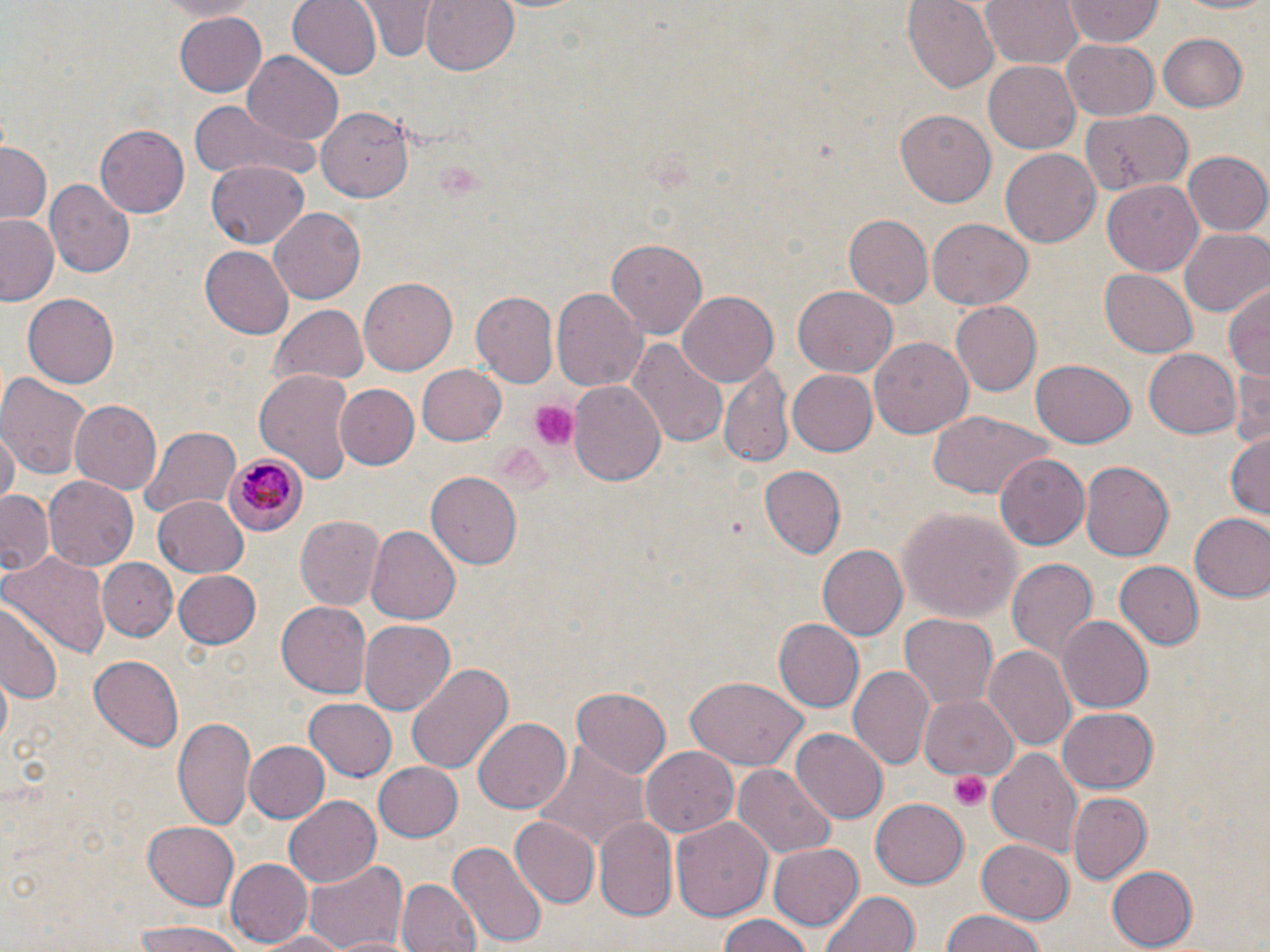

slide-level diagnosis = Plasmodium malariae
preparation = thin blood film
stain = May-Grünwald-Giemsa
field of view = single
Plasmodium malariae-infected red blood cell locations = approximate bounding boxes as (x1,y1)-(x2,y2) corner pairs in pixels: (222,453)-(304,537)
platelet locations = approximate bounding boxes as (x1,y1)-(x2,y2) corner pairs in pixels: (527,401)-(577,452), (950,772)-(990,812)
uninfected red blood cell locations = approximate bounding boxes as (x1,y1)-(x2,y2) corner pairs in pixels: (286,0)-(382,80), (421,0)-(520,75), (902,0)-(1000,92), (982,0)-(1082,70), (1165,0)-(1270,15), (362,1)-(435,61), (1063,1)-(1164,46), (172,12)-(267,97), (1155,33)-(1249,112), (1063,40)-(1159,120), (243,52)-(344,145), (982,60)-(1083,154), (189,101)-(325,185), (319,106)-(417,201), (895,106)-(995,204), (1079,108)-(1192,194), (95,124)-(188,217), (1,141)-(53,225), (1001,148)-(1100,249), (1183,152)-(1270,236), (205,161)-(310,246), (1102,178)-(1203,275), (46,179)-(135,277), (268,206)-(367,303), (844,212)-(936,306), (1,214)-(62,306), (928,219)-(1032,310), (1179,228)-(1269,315), (602,238)-(708,338), (199,246)-(294,339), (1100,269)-(1197,357), (358,277)-(456,374), (1227,281)-(1270,380), (792,286)-(897,378), (551,289)-(644,393), (676,290)-(780,385), (470,291)-(559,390), (23,294)-(118,387), (948,301)-(1040,395), (271,304)-(369,386), (629,337)-(728,452), (869,338)-(972,438), (1144,349)-(1242,439), (1030,358)-(1135,448), (414,363)-(507,447), (1231,363)-(1270,455), (719,366)-(793,470), (255,369)-(355,482), (786,369)-(877,456), (0,372)-(89,480), (567,380)-(667,487), (336,383)-(419,469), (70,397)-(164,495), (928,412)-(1051,500), (137,424)-(243,523), (1,432)-(18,509), (1226,432)-(1270,521), (994,451)-(1090,552), (1080,461)-(1174,561), (757,465)-(846,561), (427,472)-(523,569), (43,476)-(138,571), (1,491)-(57,577), (152,496)-(247,577), (899,506)-(1022,623), (1188,512)-(1270,601), (295,516)-(385,611), (366,524)-(464,624), (818,545)-(908,642), (2,548)-(110,656), (98,556)-(176,639), (1006,557)-(1099,668), (1114,561)-(1205,649), (172,570)-(262,649), (275,598)-(371,695), (0,601)-(65,707), (898,613)-(999,712), (1056,615)-(1153,714), (358,618)-(454,713), (772,619)-(864,713), (982,645)-(1076,751), (90,655)-(183,751), (405,662)-(512,776), (848,666)-(935,770), (684,678)-(808,770), (574,685)-(671,778), (919,692)-(1018,779), (304,698)-(397,782), (1058,708)-(1158,791), (173,714)-(257,833), (473,716)-(572,814), (790,729)-(886,823), (243,740)-(329,823), (529,744)-(649,854), (642,746)-(738,838), (989,747)-(1084,860), (373,761)-(465,841), (733,763)-(836,857), (1068,791)-(1152,883), (283,796)-(382,886), (871,800)-(968,886), (595,814)-(678,919), (671,815)-(773,924), (510,816)-(600,908), (143,820)-(243,910), (978,839)-(1074,921), (450,840)-(546,947), (769,840)-(864,930), (303,858)-(408,950), (225,859)-(313,946), (1108,866)-(1197,947), (397,878)-(479,952), (820,890)-(920,952), (937,910)-(1050,952), (715,915)-(820,952), (129,922)-(249,952), (257,930)-(352,952)
magnification = 1000x
image size = 1270×952 pixels
modality = optical microscopy